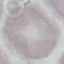
Summary:
  - Result: negative for malaria parasites
  - Preparation: thin blood smear
  - Image type: cell patch, automatically extracted from a larger field of view and resized to 64 × 64 pixels
  - Capture: smartphone camera at the microscope eyepiece
  - Stain: Giemsa